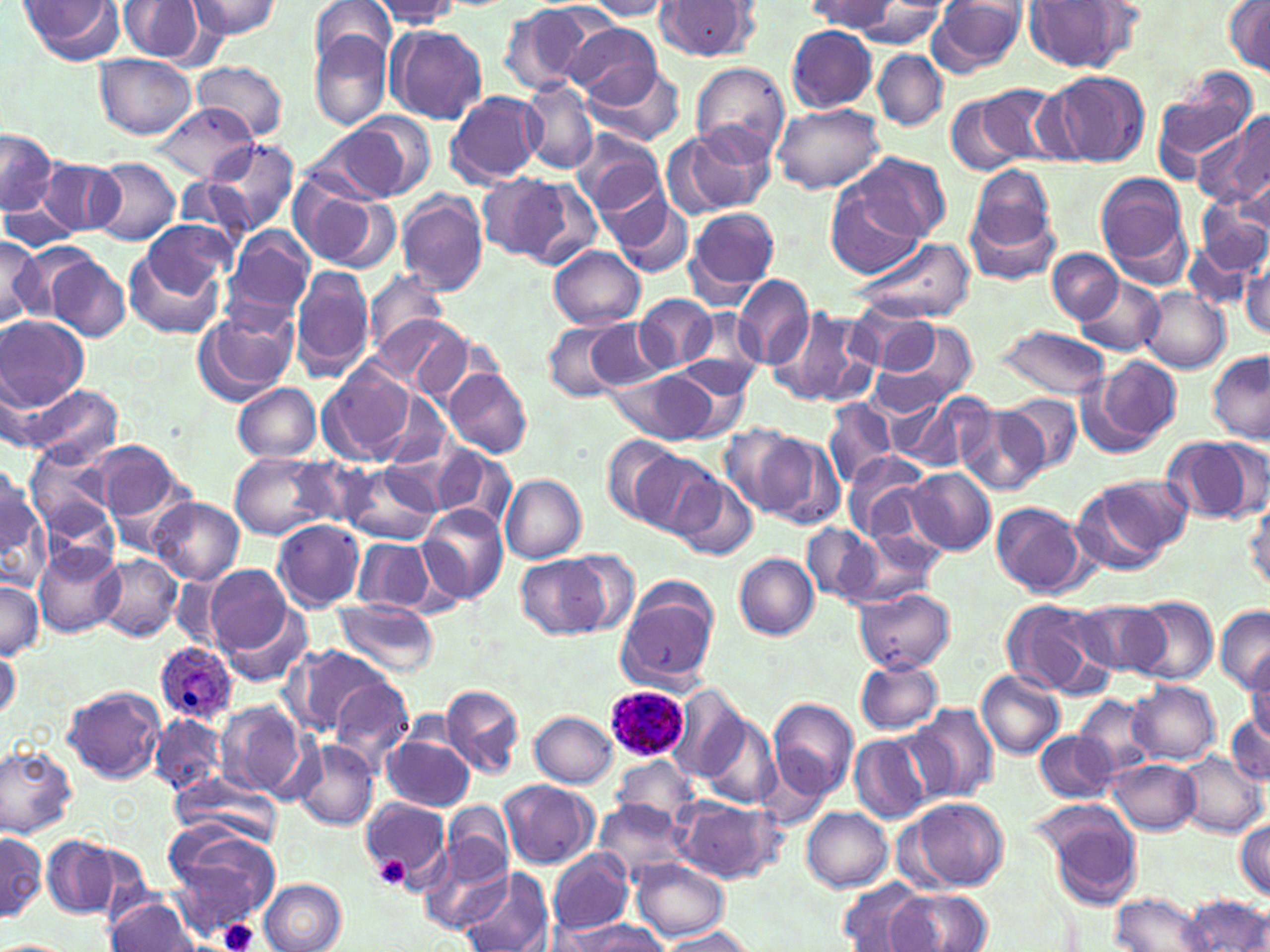
Approximate bounding boxes as [x1, y1, x2, y2] in pixels. Uninfected red blood cell locations: [15, 0, 125, 66], [117, 0, 215, 64], [185, 0, 282, 41], [310, 0, 397, 69], [583, 1, 678, 19], [653, 1, 760, 63], [810, 1, 897, 34], [929, 1, 1027, 78], [1024, 1, 1139, 74], [370, 2, 464, 29], [497, 2, 602, 96], [854, 2, 944, 49], [1225, 2, 1270, 76], [566, 23, 662, 107], [386, 25, 487, 124], [786, 25, 880, 112], [309, 30, 393, 131], [873, 50, 946, 130], [94, 54, 197, 139], [192, 61, 288, 140], [690, 61, 791, 162], [583, 63, 688, 147], [1151, 68, 1259, 179], [1045, 71, 1150, 166], [520, 79, 599, 176], [975, 85, 1071, 168], [445, 91, 545, 186], [945, 95, 1027, 175], [153, 103, 259, 182], [774, 103, 884, 194], [1196, 112, 1270, 210], [351, 113, 438, 196], [303, 122, 419, 204], [681, 124, 775, 213], [0, 127, 56, 217], [570, 128, 666, 216], [205, 137, 300, 236], [838, 152, 950, 247], [38, 158, 124, 237], [93, 158, 180, 245], [965, 164, 1058, 271], [1095, 172, 1192, 280], [475, 174, 575, 264], [516, 178, 602, 269], [288, 179, 395, 272], [823, 179, 932, 281], [397, 190, 490, 296], [610, 193, 693, 278], [1, 199, 82, 251], [1197, 204, 1270, 276], [685, 207, 779, 298], [136, 219, 235, 303], [1187, 222, 1262, 309], [224, 226, 315, 322], [850, 235, 976, 323], [0, 236, 46, 327], [124, 246, 224, 340], [550, 246, 644, 329], [1046, 249, 1123, 323], [45, 252, 129, 341], [1240, 259, 1270, 341], [292, 265, 374, 381], [363, 269, 448, 357], [733, 275, 815, 368], [1073, 277, 1166, 358], [1140, 287, 1229, 372], [633, 292, 718, 372], [193, 305, 299, 406], [853, 306, 941, 376], [767, 307, 868, 407], [674, 312, 764, 395], [375, 314, 468, 393], [0, 316, 88, 408], [543, 316, 637, 402], [867, 319, 981, 418], [588, 320, 668, 389], [993, 325, 1113, 398], [1208, 349, 1270, 446], [1084, 355, 1180, 454], [663, 358, 755, 439], [319, 363, 417, 465], [443, 369, 531, 457], [609, 369, 719, 445], [234, 383, 323, 462], [19, 384, 123, 465], [913, 391, 999, 476], [375, 393, 451, 473], [1003, 393, 1081, 474], [823, 398, 895, 488], [957, 405, 1049, 496], [721, 426, 812, 515], [1159, 436, 1260, 524], [603, 437, 681, 523], [759, 437, 845, 529], [25, 442, 117, 535], [92, 442, 182, 523], [430, 445, 515, 530], [842, 450, 929, 542], [229, 451, 337, 539], [631, 451, 721, 535], [340, 461, 440, 545], [0, 465, 46, 582], [904, 468, 993, 554], [1073, 473, 1188, 572], [501, 475, 586, 562], [671, 475, 756, 561], [148, 497, 245, 585], [1247, 498, 1270, 594], [992, 501, 1088, 596], [421, 504, 508, 602], [272, 519, 364, 610], [802, 522, 884, 602], [820, 529, 928, 610], [352, 537, 437, 614], [34, 546, 123, 637], [557, 551, 641, 634], [733, 552, 819, 639], [95, 554, 182, 641], [518, 555, 607, 638], [203, 565, 297, 656], [170, 575, 228, 647], [0, 579, 43, 660], [616, 587, 718, 688], [853, 587, 954, 674], [1128, 595, 1218, 686], [331, 599, 440, 677], [998, 599, 1111, 697], [1068, 600, 1172, 678], [217, 603, 313, 687], [1214, 605, 1270, 691], [0, 643, 20, 722], [285, 644, 393, 737], [1247, 657, 1270, 746], [853, 659, 944, 734], [976, 668, 1066, 759], [329, 680, 412, 774], [1127, 680, 1221, 765], [668, 683, 750, 781], [441, 684, 525, 778], [62, 685, 166, 783], [1071, 693, 1158, 782], [769, 698, 857, 797], [217, 700, 306, 799], [910, 703, 999, 801], [1227, 708, 1270, 785], [530, 711, 618, 789], [699, 712, 782, 810], [151, 713, 225, 795], [1035, 729, 1120, 802], [850, 734, 934, 825], [382, 735, 475, 811], [293, 740, 380, 831], [0, 745, 78, 838], [1176, 753, 1266, 838], [612, 757, 700, 824], [1105, 760, 1200, 834], [172, 772, 282, 844], [500, 780, 597, 869], [359, 795, 452, 889], [671, 796, 785, 884], [909, 797, 1009, 891], [1033, 798, 1145, 908], [596, 799, 691, 880], [441, 801, 513, 883], [802, 807, 893, 891], [1233, 818, 1270, 899], [165, 827, 284, 930], [0, 829, 49, 921], [41, 837, 121, 918], [422, 840, 513, 935], [548, 849, 634, 936], [631, 857, 727, 941], [458, 868, 554, 952], [260, 878, 346, 952], [839, 879, 929, 951], [888, 888, 993, 950], [1109, 892, 1213, 951], [105, 893, 198, 951], [1185, 895, 1269, 951], [558, 918, 666, 952], [657, 928, 758, 952], [0, 938, 76, 952]. Platelet locations: [374, 856, 409, 889], [215, 917, 261, 952]. Plasmodium ovale-infected red blood cell locations: [154, 642, 237, 724], [606, 684, 688, 764]. Slide-level diagnosis: Plasmodium ovale. Image is 1270×952 pixels. Thin blood film. 1000x magnification. May-Grünwald-Giemsa-stained preparation. Single field of view. Light microscopy.